State the blood parasite species.
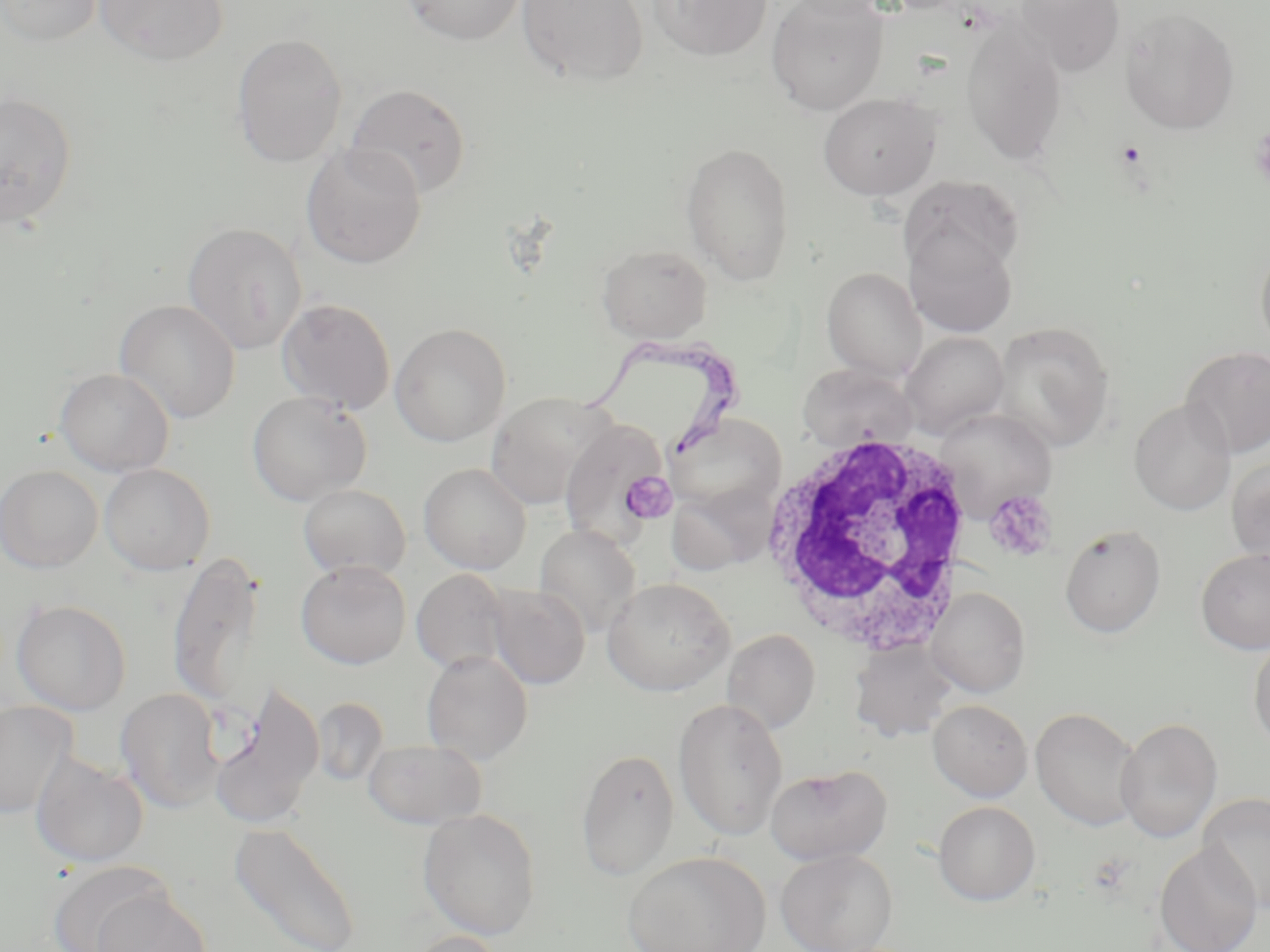

Trypanosoma brucei.

Approximate bounding boxes as (x1, y1, x2, y2) in pixels. Uninfected red blood cell locations: (1, 0, 103, 46), (93, 0, 229, 66), (401, 0, 526, 45), (517, 0, 649, 86), (648, 0, 773, 61), (766, 0, 889, 115), (781, 0, 892, 19), (1015, 0, 1125, 75), (1120, 9, 1240, 134), (960, 26, 1067, 164), (231, 33, 348, 168), (345, 83, 471, 199), (0, 92, 78, 229), (818, 93, 941, 200), (680, 141, 795, 285), (300, 143, 428, 269), (901, 175, 1025, 282), (182, 221, 307, 355), (904, 223, 1018, 338), (1255, 238, 1270, 359), (597, 243, 713, 342), (821, 267, 927, 381), (276, 297, 396, 414), (115, 300, 241, 424), (991, 322, 1116, 451), (390, 323, 511, 447), (900, 331, 1009, 439), (1181, 346, 1270, 458), (797, 363, 918, 451), (54, 368, 174, 476), (246, 391, 373, 507), (484, 391, 611, 509), (1129, 398, 1236, 516), (934, 407, 1056, 516), (665, 412, 787, 519), (559, 417, 672, 547), (1226, 458, 1270, 565), (99, 463, 215, 575), (419, 463, 531, 574), (0, 465, 103, 573), (297, 477, 535, 577), (298, 483, 410, 580), (1059, 524, 1166, 638), (534, 525, 641, 636), (1196, 547, 1270, 654), (167, 550, 264, 710), (295, 560, 411, 669), (411, 568, 510, 674), (602, 577, 735, 696), (487, 584, 590, 690), (927, 587, 1030, 698), (11, 599, 132, 715), (722, 630, 821, 734), (1248, 636, 1270, 752), (848, 639, 961, 743), (421, 651, 533, 764), (208, 685, 324, 830), (115, 687, 225, 813), (310, 697, 389, 788), (673, 697, 789, 841), (927, 699, 1032, 800), (0, 701, 79, 820), (1031, 707, 1143, 831), (1115, 717, 1222, 843), (363, 738, 487, 829), (576, 748, 680, 881), (30, 753, 149, 868), (765, 764, 893, 865), (1198, 793, 1270, 913), (933, 801, 1040, 906), (418, 808, 541, 940), (228, 822, 362, 952), (1154, 842, 1264, 952), (775, 849, 897, 952), (622, 851, 770, 952), (46, 862, 172, 952), (90, 890, 212, 952), (406, 931, 507, 952). Platelet locations: (621, 470, 680, 522), (984, 488, 1058, 562). Trypanosoma brucei locations: (575, 328, 752, 461). White blood cell locations: (757, 426, 975, 658). Image is 1270×952 pixels. 1000x magnification. Light microscopy. Thin blood smear. Single field of view. May-Grünwald-Giemsa stain.